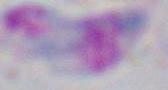 Micrograph. Toxoplasma gondii is seen. Captured at 1000x magnification.